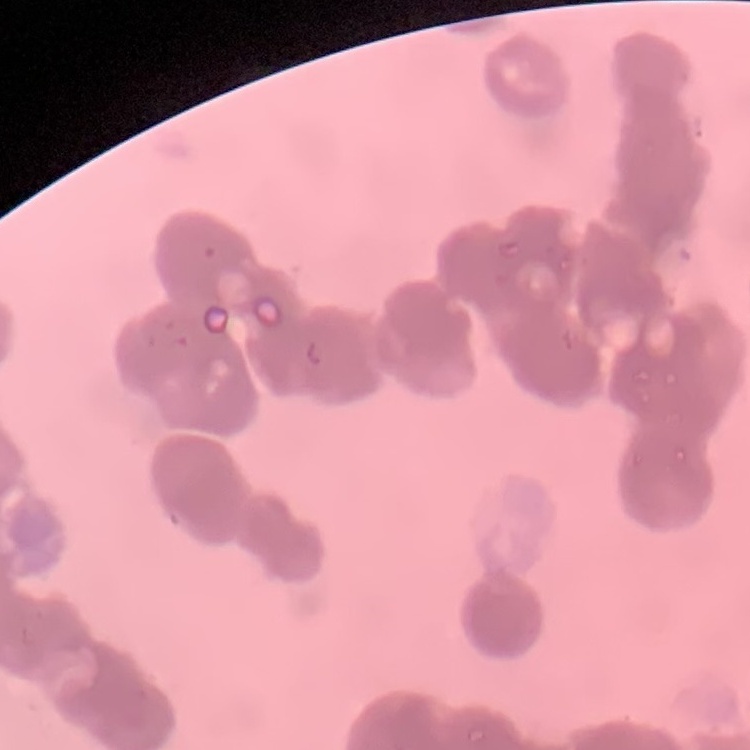

Summary:
  - Red blood cell morphology: rouleaux formation
  - Image type: one tile cut from a larger photomicrograph
  - Preparation: thin peripheral smear
  - Stain: Field's or Giemsa